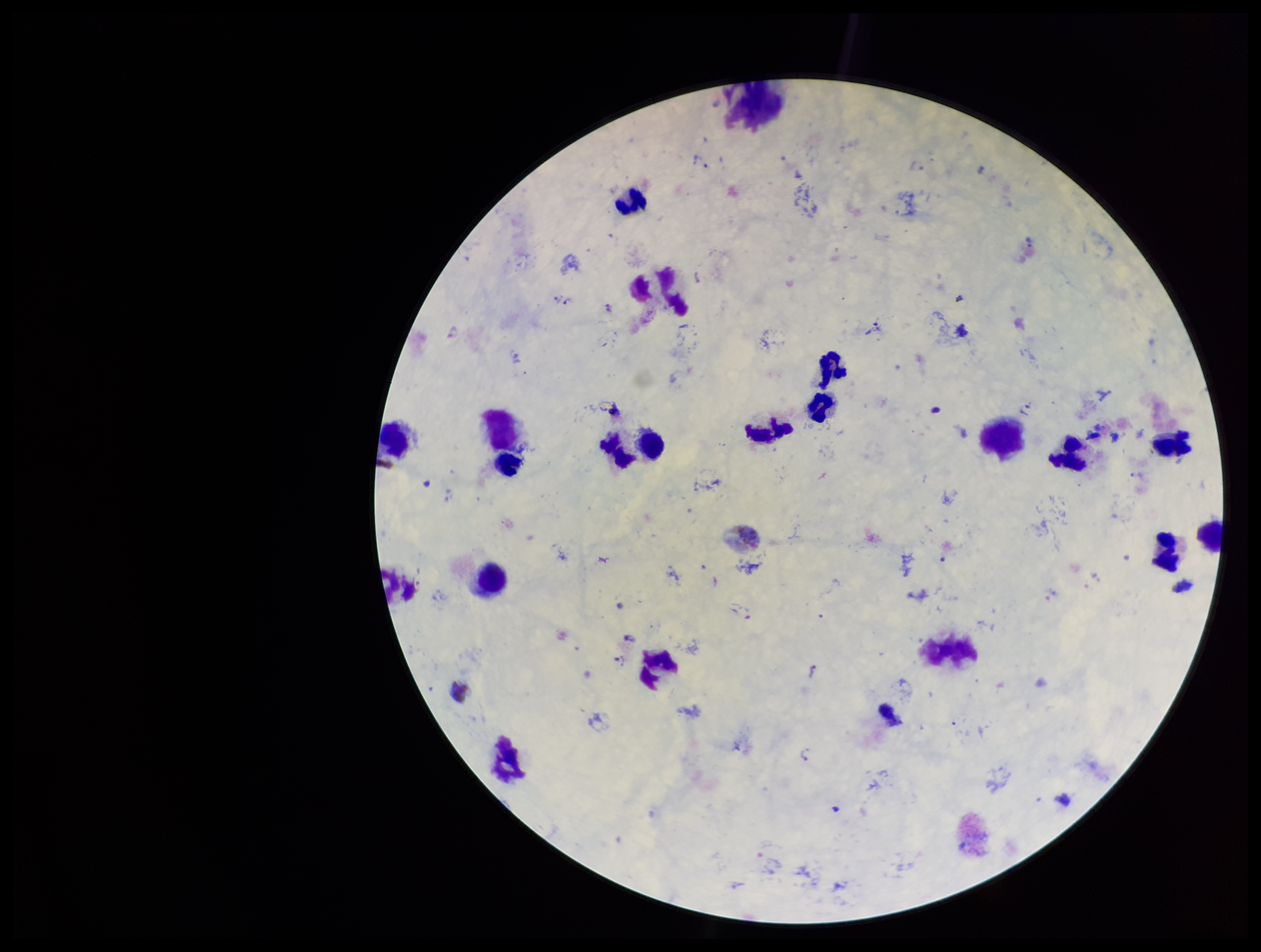

patient malaria status = infected
image size = 1261×952 pixels
preparation = thick
parasite count = 5
capture = smartphone photograph through the microscope eyepiece
species reported for this patient = Plasmodium vivax
stain = Giemsa
leukocyte count = 15
Plasmodium parasites = identified
field of view = single